Assess this cell for malaria.
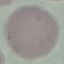
It is uninfected.

Thin smear of blood. Cell patch, automatically extracted from a larger field of view and resized to 64 × 64 pixels. Photographed with a smartphone camera at the microscope eyepiece. Giemsa-stained preparation.